Comment on the morphology of the red blood cells.
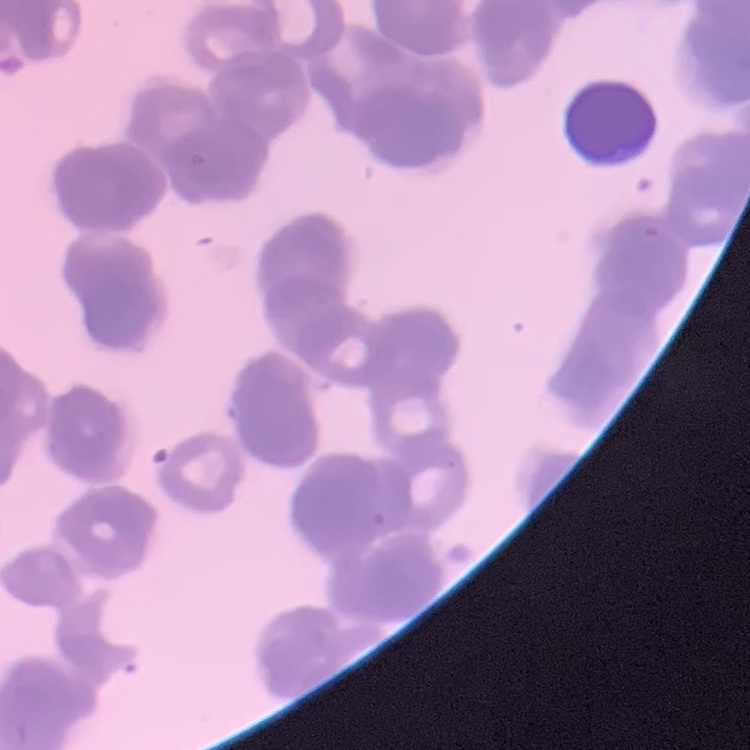
Rouleaux formation.

image type = one tile cut from a larger photomicrograph
stain = Field's or Giemsa
preparation = thin peripheral smear